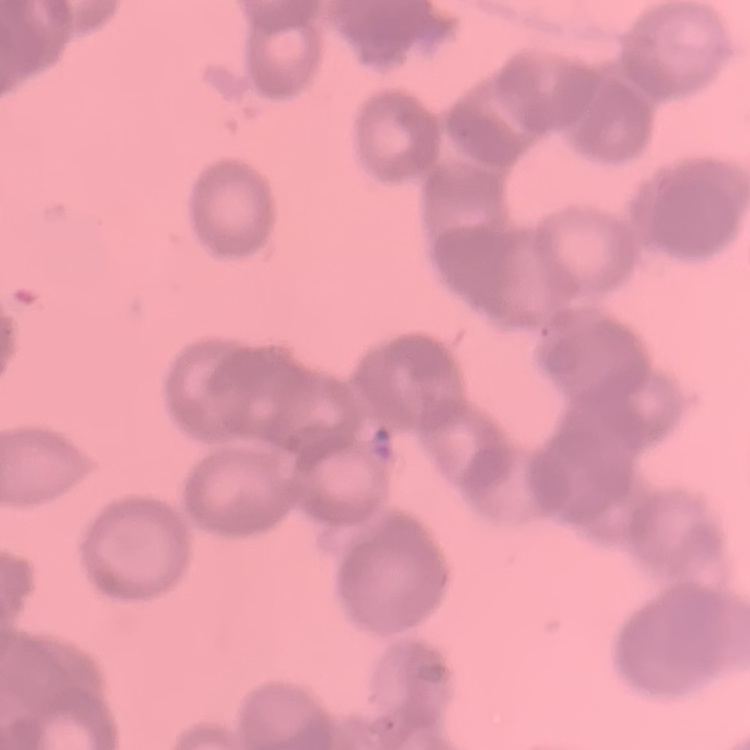
red blood cell morphology = rouleaux formation
preparation = thin blood film
image type = one tile cut from a larger photomicrograph
stain = Field's or Giemsa